Locate platelets.
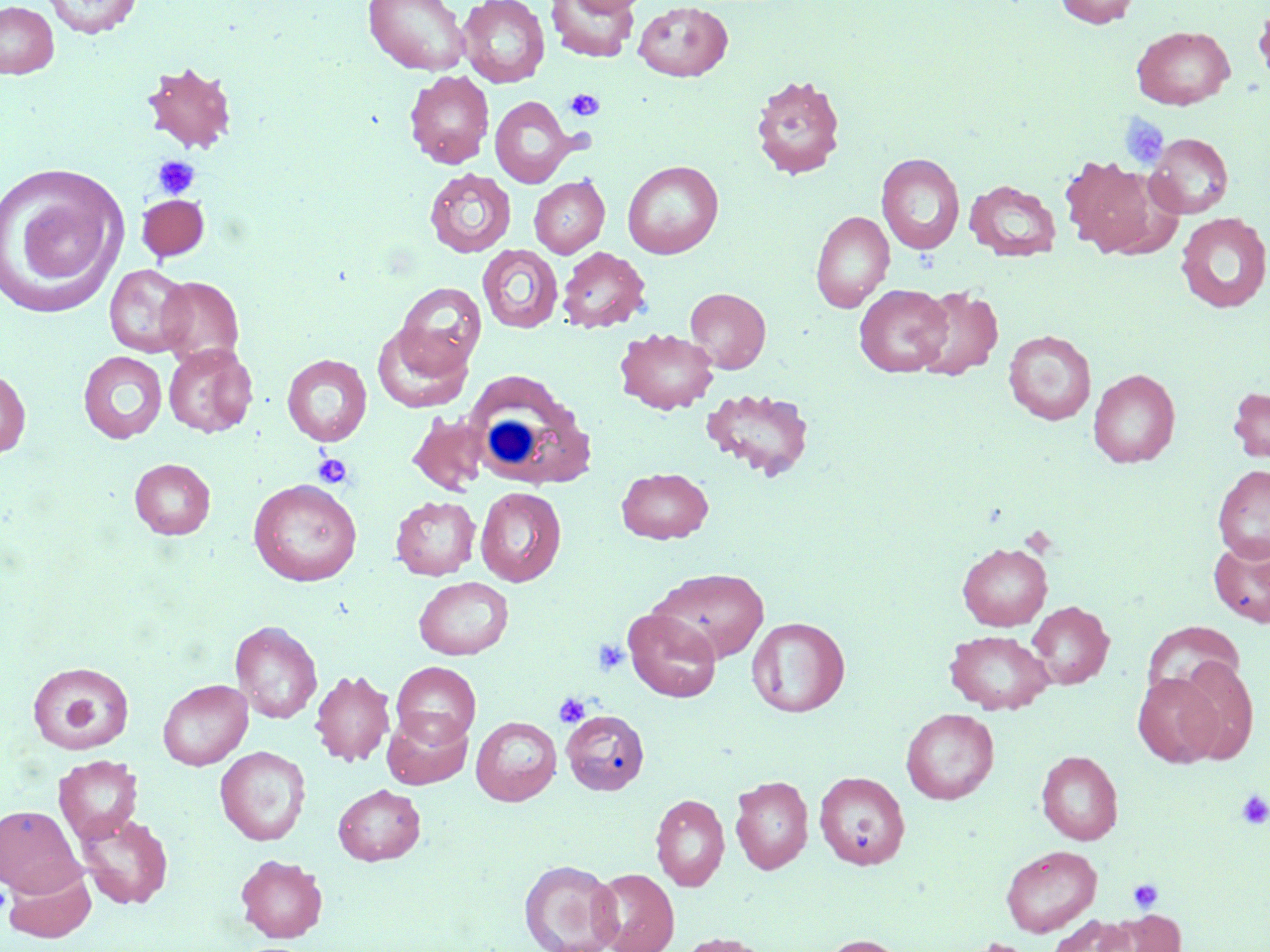
Approximate bounding boxes as named x1/y1/x2/y2 corners in pixels.
Platelets: (x1=565, y1=89, x2=604, y2=121), (x1=1119, y1=114, x2=1170, y2=171), (x1=152, y1=155, x2=200, y2=200), (x1=312, y1=452, x2=354, y2=489), (x1=593, y1=639, x2=629, y2=676), (x1=57, y1=685, x2=106, y2=736), (x1=554, y1=693, x2=590, y2=727), (x1=1236, y1=791, x2=1270, y2=829), (x1=1128, y1=878, x2=1163, y2=914), (x1=965, y1=938, x2=1039, y2=952).

slide_level_diagnosis: negative for blood parasites
preparation: thin blood film
field_of_view: one of a larger specimen
image_size: 1270×952 pixels
stain: May-Grünwald-Giemsa
white_blood_cell_locations: 'approximate bounding boxes as named x1/y1/x2/y2 corners in pixels: (x1=464, y1=371, x2=596, y2=492)'
modality: optical microscopy
magnification: 1000x
uninfected_red_blood_cell_locations: 'approximate bounding boxes as named x1/y1/x2/y2 corners in pixels: (x1=41, y1=0, x2=143, y2=38), (x1=363, y1=0, x2=470, y2=75), (x1=457, y1=0, x2=550, y2=87), (x1=546, y1=0, x2=639, y2=62), (x1=566, y1=0, x2=650, y2=16), (x1=1055, y1=0, x2=1141, y2=28), (x1=0, y1=1, x2=59, y2=78), (x1=633, y1=1, x2=733, y2=82), (x1=1253, y1=3, x2=1270, y2=85), (x1=1131, y1=26, x2=1235, y2=109), (x1=141, y1=61, x2=237, y2=154), (x1=404, y1=70, x2=494, y2=169), (x1=750, y1=73, x2=846, y2=181), (x1=490, y1=96, x2=577, y2=187), (x1=1146, y1=133, x2=1234, y2=218), (x1=877, y1=154, x2=965, y2=254), (x1=1059, y1=155, x2=1169, y2=258), (x1=623, y1=160, x2=723, y2=259), (x1=1, y1=165, x2=125, y2=315), (x1=424, y1=168, x2=516, y2=257), (x1=529, y1=176, x2=609, y2=258), (x1=965, y1=180, x2=1061, y2=261), (x1=136, y1=194, x2=210, y2=262), (x1=810, y1=211, x2=894, y2=313), (x1=1176, y1=213, x2=1270, y2=313), (x1=477, y1=244, x2=563, y2=334), (x1=556, y1=246, x2=651, y2=333), (x1=105, y1=264, x2=194, y2=357), (x1=156, y1=276, x2=244, y2=367), (x1=394, y1=281, x2=486, y2=378), (x1=854, y1=284, x2=952, y2=376), (x1=912, y1=285, x2=1003, y2=381), (x1=685, y1=287, x2=770, y2=372), (x1=372, y1=324, x2=472, y2=412), (x1=615, y1=327, x2=718, y2=415), (x1=1004, y1=330, x2=1096, y2=425), (x1=163, y1=344, x2=257, y2=437), (x1=78, y1=351, x2=168, y2=443), (x1=281, y1=354, x2=372, y2=446), (x1=0, y1=367, x2=31, y2=459), (x1=1088, y1=368, x2=1180, y2=467), (x1=701, y1=386, x2=815, y2=481), (x1=1227, y1=387, x2=1270, y2=463), (x1=406, y1=411, x2=490, y2=496), (x1=129, y1=458, x2=215, y2=539), (x1=1212, y1=465, x2=1270, y2=562), (x1=617, y1=467, x2=713, y2=543), (x1=248, y1=479, x2=362, y2=586), (x1=475, y1=487, x2=566, y2=586), (x1=391, y1=495, x2=480, y2=580), (x1=1209, y1=535, x2=1270, y2=627), (x1=958, y1=542, x2=1052, y2=630), (x1=649, y1=567, x2=769, y2=663), (x1=414, y1=576, x2=513, y2=660), (x1=1027, y1=600, x2=1114, y2=689), (x1=623, y1=608, x2=722, y2=703), (x1=747, y1=616, x2=849, y2=717), (x1=230, y1=620, x2=322, y2=723), (x1=1143, y1=620, x2=1246, y2=703), (x1=944, y1=629, x2=1054, y2=714), (x1=1173, y1=655, x2=1259, y2=764), (x1=27, y1=661, x2=135, y2=755), (x1=392, y1=662, x2=481, y2=747), (x1=310, y1=670, x2=395, y2=767), (x1=1132, y1=672, x2=1224, y2=768), (x1=157, y1=679, x2=252, y2=770), (x1=900, y1=708, x2=999, y2=804), (x1=561, y1=710, x2=649, y2=795), (x1=382, y1=711, x2=473, y2=789), (x1=471, y1=716, x2=562, y2=805), (x1=215, y1=746, x2=311, y2=845), (x1=1037, y1=750, x2=1123, y2=844), (x1=53, y1=755, x2=143, y2=845), (x1=814, y1=771, x2=909, y2=869), (x1=730, y1=775, x2=813, y2=874), (x1=333, y1=784, x2=426, y2=865), (x1=651, y1=794, x2=730, y2=891), (x1=0, y1=805, x2=83, y2=896), (x1=75, y1=811, x2=174, y2=910), (x1=1001, y1=844, x2=1102, y2=936), (x1=235, y1=855, x2=328, y2=942), (x1=519, y1=859, x2=622, y2=952), (x1=3, y1=862, x2=96, y2=944), (x1=590, y1=868, x2=679, y2=952), (x1=1099, y1=911, x2=1185, y2=952), (x1=1045, y1=915, x2=1136, y2=952), (x1=672, y1=933, x2=776, y2=952), (x1=817, y1=934, x2=914, y2=952)'